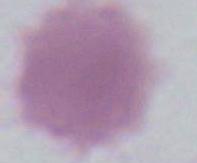
modality = micrograph
magnification = 1000x
identification = red blood cell